Assess this cell for malaria.
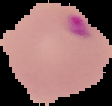

It is parasitized.

Image is 112×106 pixels. The area outside the segmented cell region is set to black. From a thin blood film.